Describe the morphology of the erythrocytes.
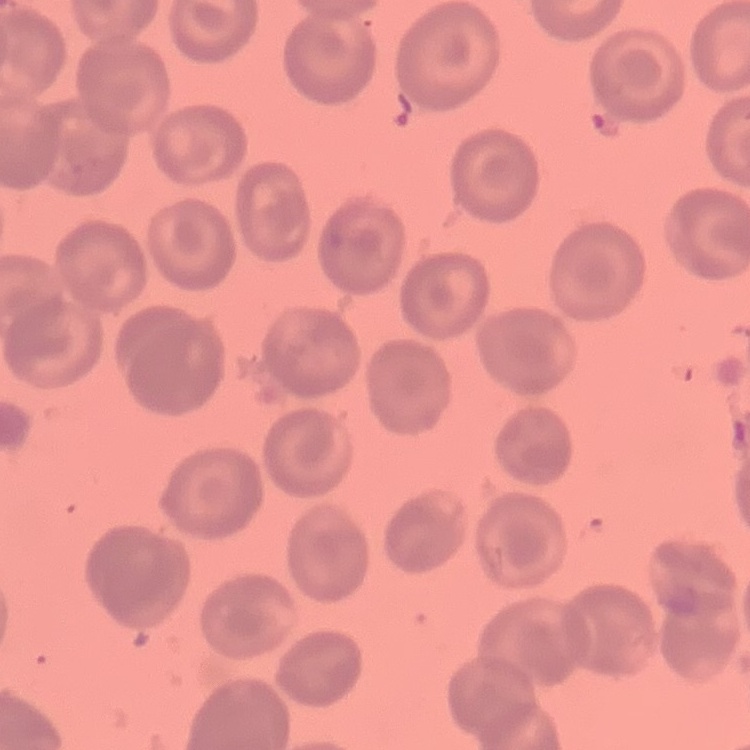

They show no rouleaux formation.

Field's or Giemsa stain. One tile cut from a larger photomicrograph. Thin blood smear.